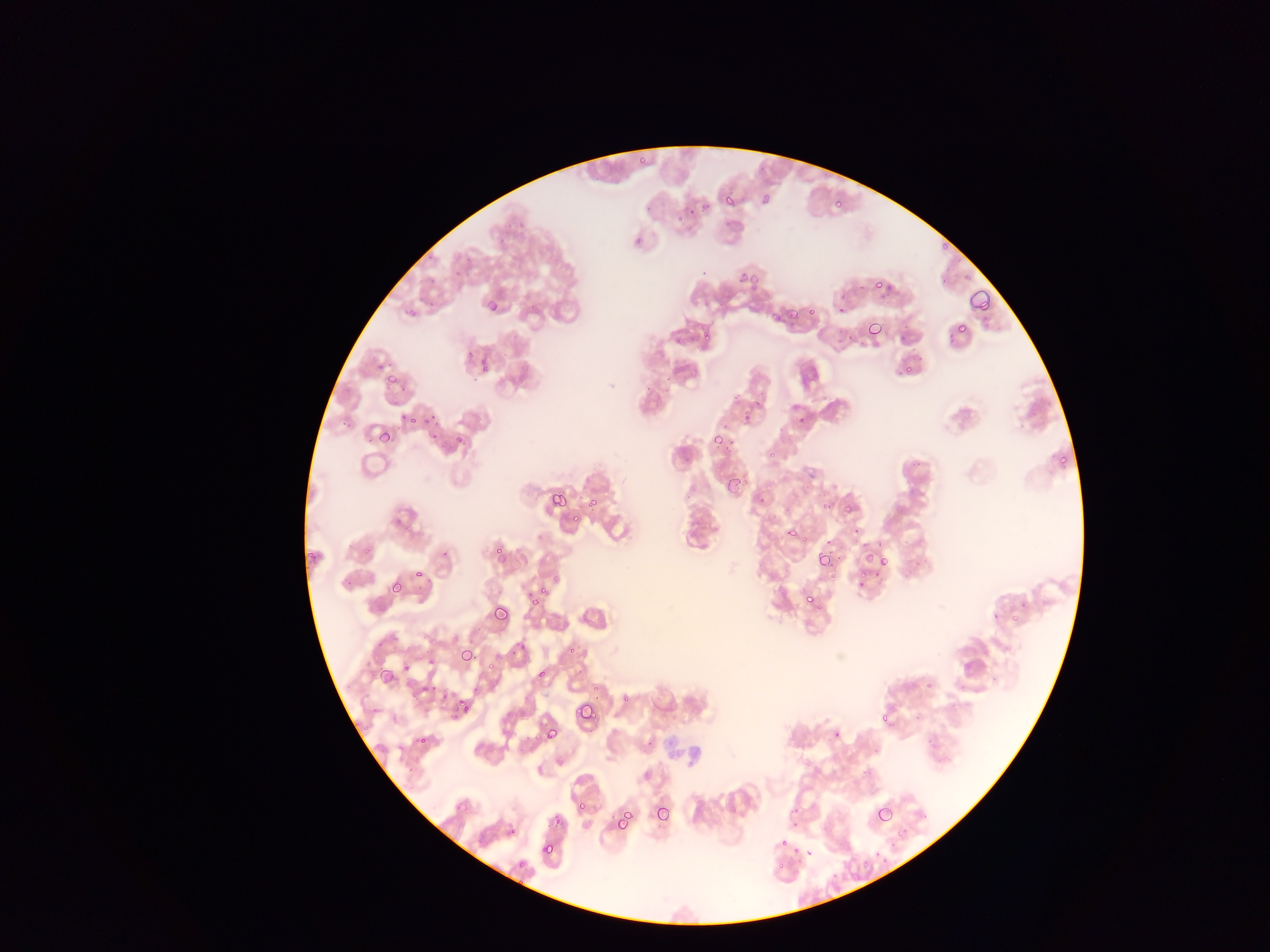

country: Ghana
capture: mobile-phone photograph through a microscope
preparation: thin blood film
malaria_parasite_locations: 'approximate bounding boxes as {left, top, right, bottom} in pixels: {635, 156, 649, 172}, {721, 191, 739, 210}, {759, 191, 775, 210}, {830, 195, 845, 211}, {690, 204, 701, 221}, {674, 215, 683, 229}, {734, 267, 760, 287}, {869, 272, 888, 289}, {967, 288, 994, 317}, {483, 295, 495, 316}, {781, 301, 815, 321}, {864, 319, 884, 341}, {952, 321, 969, 340}, {697, 328, 714, 348}, {464, 352, 473, 365}, {902, 361, 912, 375}, {380, 371, 397, 396}, {740, 406, 760, 428}, {400, 410, 421, 430}, {426, 425, 444, 446}, {377, 428, 395, 447}, {450, 431, 470, 452}, {713, 433, 735, 455}, {1054, 450, 1071, 470}, {724, 474, 745, 496}, {545, 484, 577, 515}, {548, 490, 568, 510}, {585, 493, 602, 514}, {816, 493, 836, 510}, {845, 493, 862, 518}, {785, 517, 799, 543}, {488, 531, 510, 564}, {860, 548, 878, 568}, {814, 549, 836, 571}, {864, 551, 889, 574}, {409, 562, 431, 582}, {854, 574, 870, 592}, {387, 576, 408, 599}, {526, 586, 548, 609}, {804, 593, 822, 612}, {487, 606, 511, 630}, {507, 637, 527, 664}, {459, 646, 476, 666}, {481, 656, 494, 678}, {368, 664, 385, 689}, {406, 672, 439, 704}, {572, 699, 598, 728}, {446, 702, 470, 722}, {880, 711, 900, 731}, {540, 722, 561, 746}, {410, 735, 429, 752}, {857, 763, 877, 786}, {574, 797, 586, 814}, {651, 802, 674, 828}, {873, 803, 895, 828}, {612, 808, 636, 834}, {551, 809, 566, 827}, {775, 834, 793, 852}, {540, 841, 556, 859}'
field_of_view: single
image_size: 1270×952 pixels